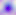

Micrograph. 400x magnification. Toxoplasma gondii is shown.